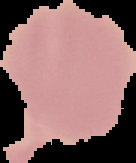
Cell region segmented out of the field of view; the surrounding area is masked to black. Result: no Plasmodium parasites detected. From a thin blood film. Image is 136×163 pixels.